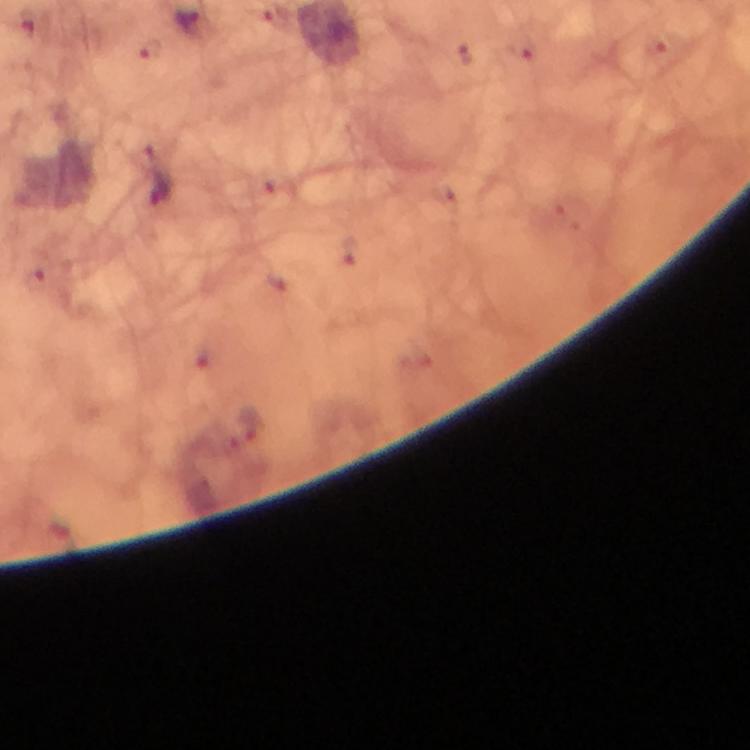
Approximate centers as {x, y} in pixels. Malaria parasite locations: {188, 22}, {159, 190}. Giemsa stain. Thick blood film. At 100x magnification. Image is 750×750 pixels. Photographed through the microscope with a smartphone camera. Immersion oil applied. From a diagnostic examination for malaria. Cropped region of a single field of view.